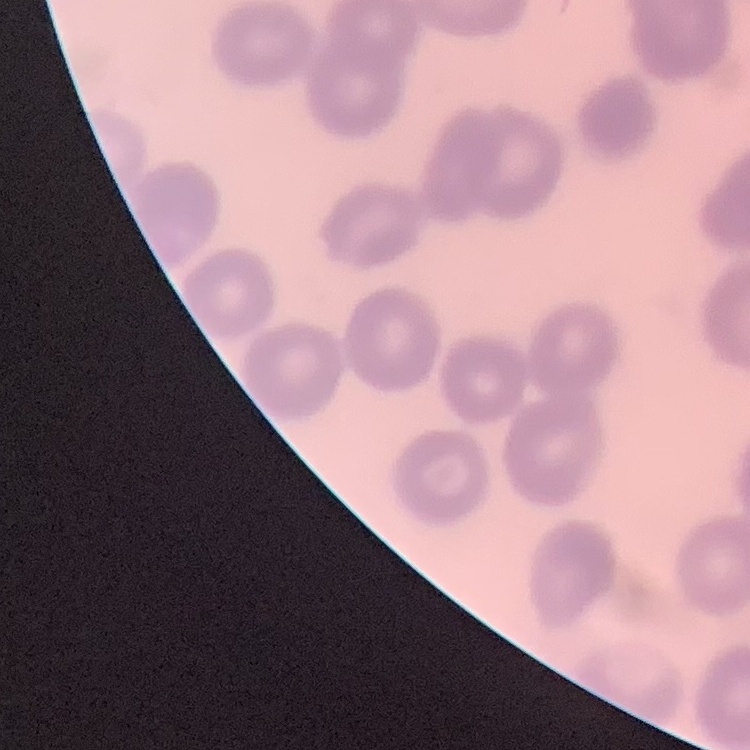
red blood cell morphology = no rouleaux formation
preparation = thin blood smear
stain = Field's or Giemsa
image type = one tile cut from a larger photomicrograph